Comment on the morphology of the erythrocytes.
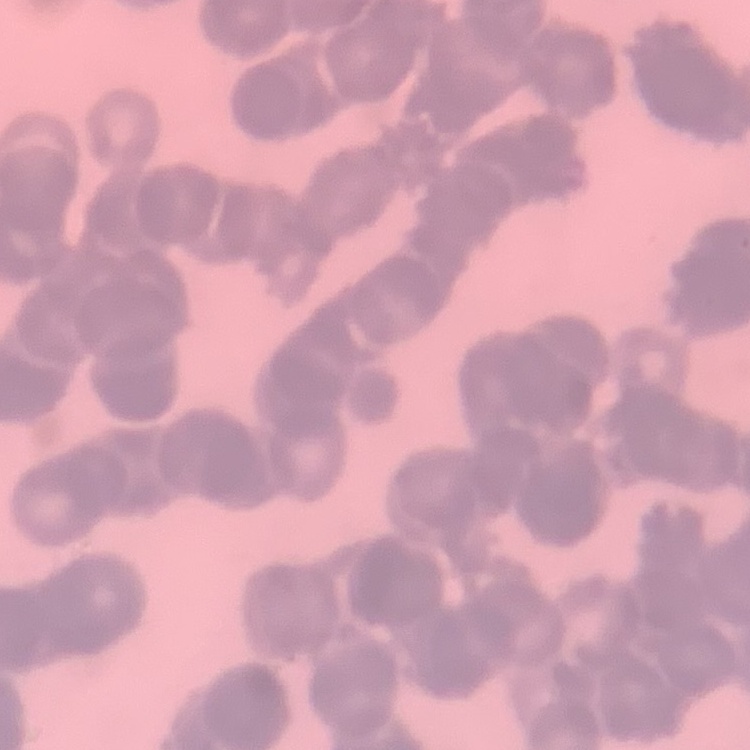

Rouleaux formation.

{
  "stain": "Field's or Giemsa",
  "image_type": "square crop of a larger photomicrograph",
  "preparation": "thin blood smear"
}